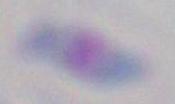

Summary:
  - Magnification: 1000x
  - Identification: Toxoplasma gondii
  - Modality: micrograph